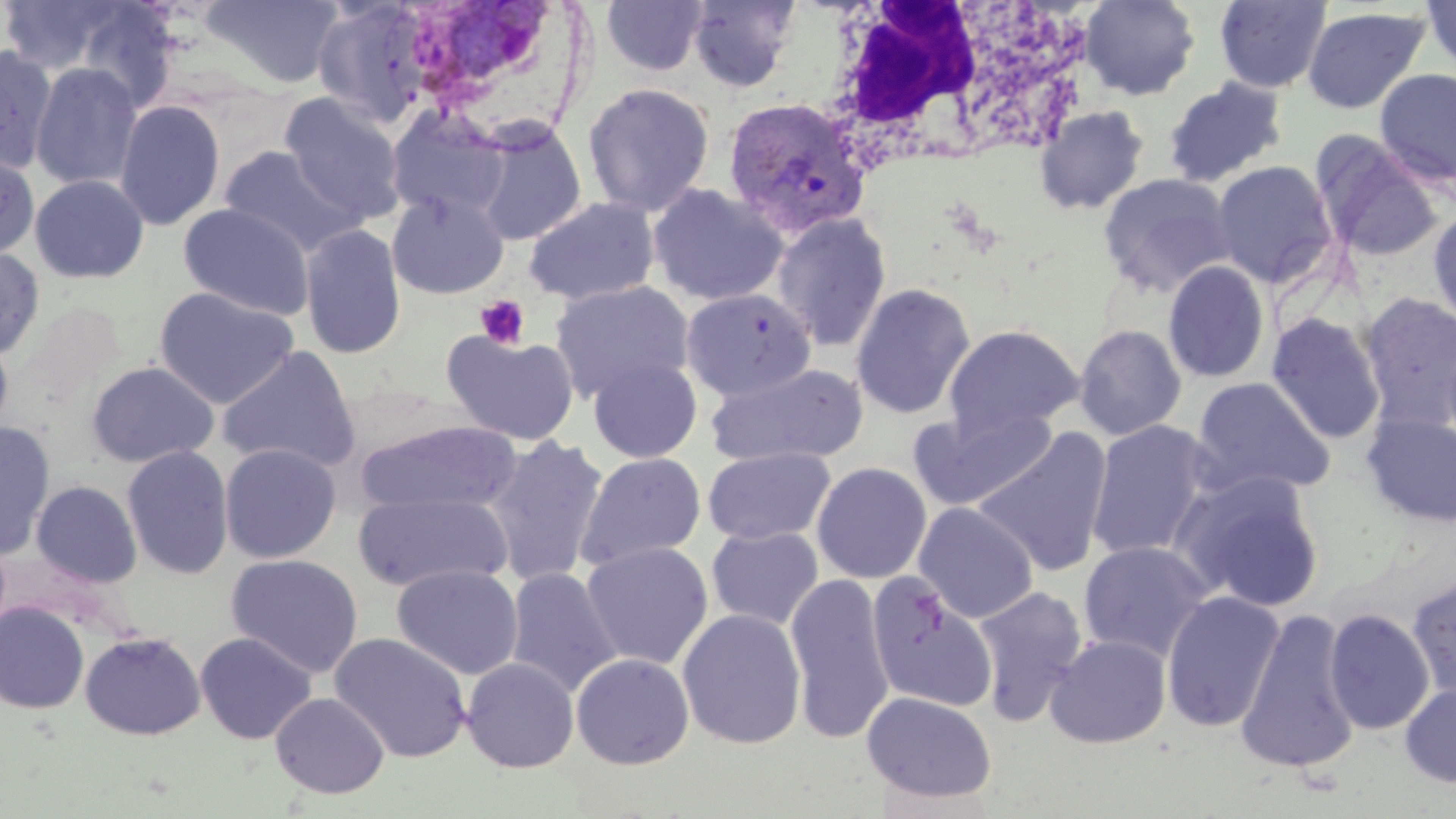

Summary:
  - Coordinate format: approximate bounding boxes as [x1, y1, x2, y2] in pixels
  - Uninfected red blood cell locations: [0, 0, 132, 75], [201, 0, 345, 88], [686, 0, 801, 93], [1080, 0, 1201, 100], [1213, 0, 1331, 93], [601, 1, 709, 76], [1420, 1, 1456, 74], [67, 2, 182, 113], [313, 2, 433, 127], [1302, 6, 1428, 114], [0, 45, 57, 173], [30, 62, 143, 191], [1375, 68, 1456, 188], [1161, 77, 1288, 188], [583, 82, 715, 217], [279, 94, 407, 224], [114, 100, 226, 231], [1034, 106, 1149, 215], [386, 109, 509, 222], [472, 121, 587, 245], [1312, 133, 1443, 263], [219, 145, 364, 256], [0, 151, 40, 261], [1212, 160, 1338, 288], [1098, 172, 1236, 297], [29, 174, 149, 284], [647, 183, 788, 306], [386, 191, 509, 299], [523, 196, 660, 306], [178, 203, 314, 321], [1428, 206, 1456, 331], [771, 212, 892, 353], [299, 223, 406, 360], [0, 247, 45, 361], [1162, 260, 1271, 384], [551, 281, 694, 402], [850, 282, 976, 419], [154, 287, 300, 410], [680, 287, 817, 401], [1359, 292, 1456, 432], [1266, 313, 1386, 444], [1074, 324, 1187, 441], [944, 325, 1083, 436], [441, 330, 580, 445], [0, 332, 14, 441], [217, 345, 361, 473], [588, 356, 702, 463], [86, 361, 219, 468], [704, 362, 867, 466], [1191, 377, 1335, 499], [911, 405, 1059, 511], [1362, 412, 1456, 527], [1086, 419, 1214, 562], [357, 420, 523, 516], [0, 422, 55, 560], [972, 427, 1113, 577], [483, 435, 609, 588], [219, 442, 341, 563], [121, 445, 234, 580], [703, 447, 835, 545], [575, 452, 706, 570], [811, 461, 932, 584], [1174, 470, 1325, 614], [31, 480, 142, 588], [353, 490, 513, 593], [913, 502, 1039, 623], [707, 526, 823, 630], [1078, 540, 1213, 663], [581, 541, 714, 670], [225, 553, 364, 678], [392, 564, 523, 680], [504, 567, 622, 698], [784, 572, 895, 745], [867, 576, 998, 713], [1407, 577, 1456, 701], [972, 585, 1088, 726], [1160, 591, 1285, 733], [0, 602, 89, 714], [677, 608, 806, 749], [1324, 608, 1434, 735], [1235, 609, 1361, 775], [80, 631, 206, 740], [195, 631, 317, 744], [330, 632, 472, 763], [1045, 633, 1172, 748], [571, 652, 694, 770], [461, 657, 579, 773], [1400, 682, 1456, 788], [862, 691, 997, 803], [270, 692, 389, 799]
  - White blood cell locations: [802, 0, 1081, 176]
  - Plasmodium vivax-infected red blood cell locations: [445, 1, 564, 88], [721, 96, 871, 239]
  - Platelet locations: [474, 294, 530, 350]
  - Slide-level diagnosis: Plasmodium vivax
  - Modality: light microscopy
  - Stain: May-Grünwald-Giemsa
  - Image size: 1456×819 pixels
  - Field of view: one of a larger specimen
  - Preparation: thin blood smear
  - Magnification: 1000x